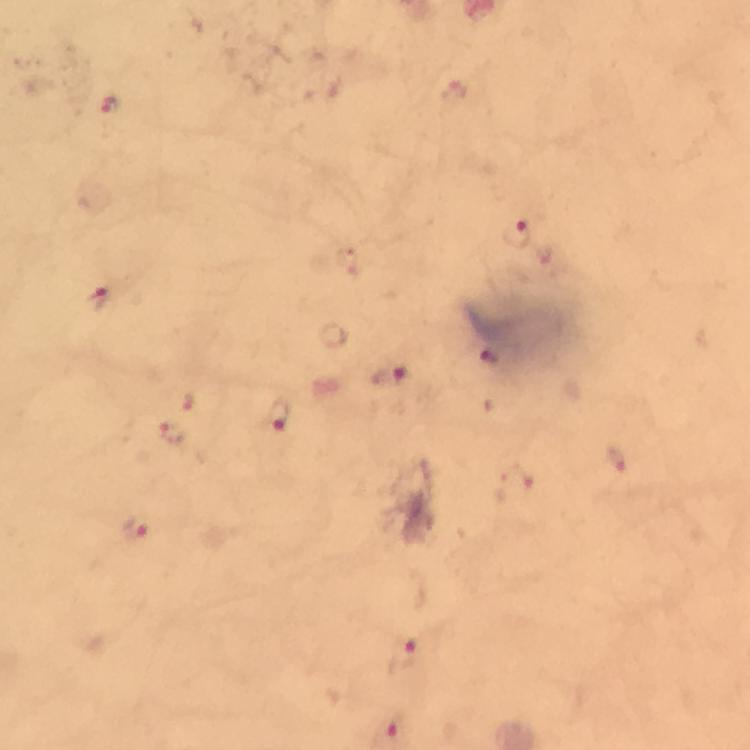

Approximate centers as [x, y] in pixels. Plasmodium parasite locations: [108, 106], [517, 233], [97, 297], [489, 362], [389, 375], [281, 416], [174, 432], [615, 456], [513, 485], [133, 530], [403, 656]. A crop from one field of view. Photographed through the microscope with a smartphone camera. Thick smear. Giemsa-stained preparation. From a diagnostic examination for malaria. Image is 750×750 pixels. At 100x magnification. Immersion oil was used.